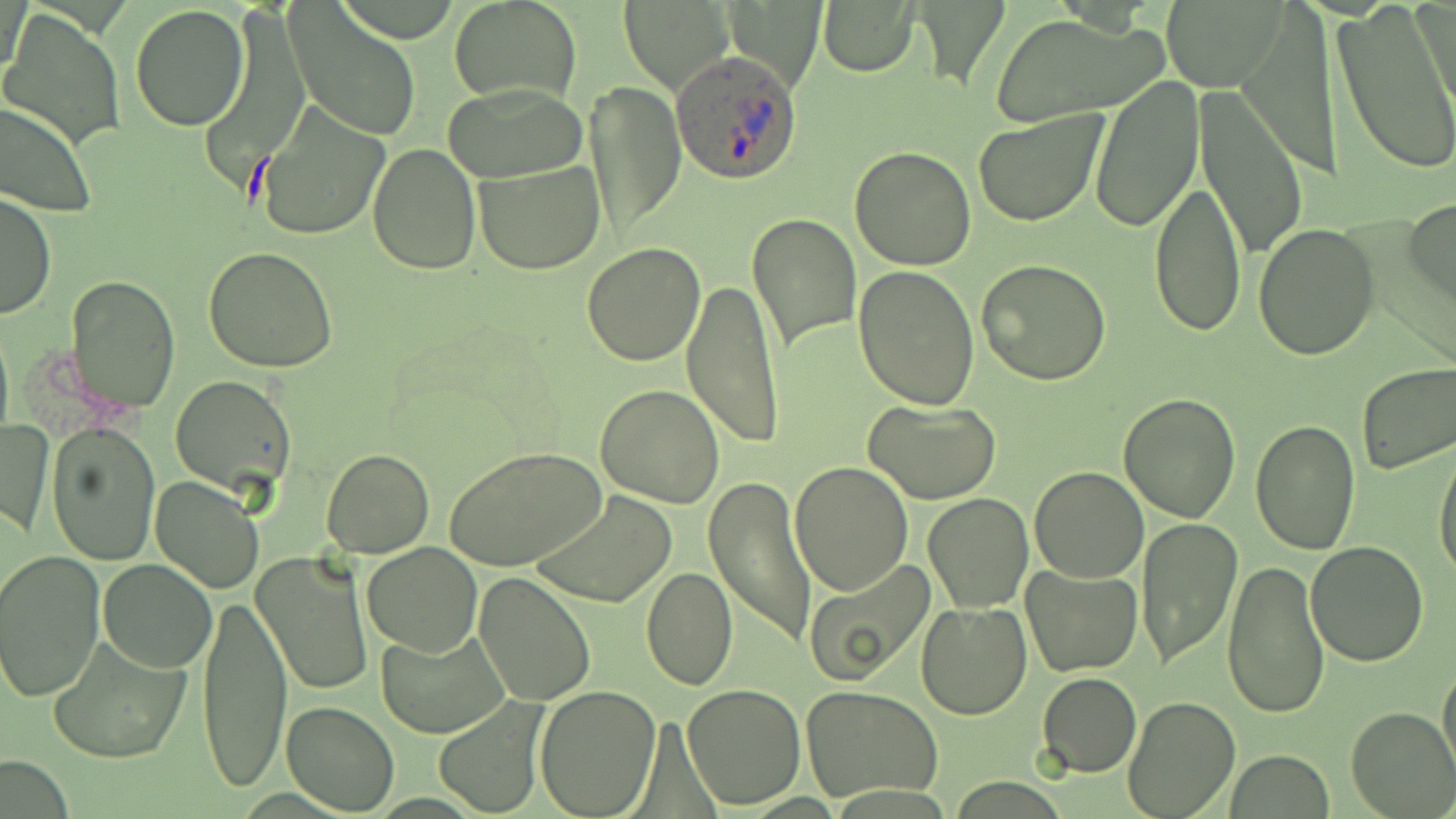
Summary:
  - Coordinate format: approximate bounding boxes as (x1, y1, x2, y2) in pixels
  - Uninfected red blood cell locations: (818, 0, 920, 76), (1414, 0, 1454, 119), (447, 1, 584, 107), (1332, 1, 1456, 178), (618, 2, 735, 96), (1161, 2, 1287, 90), (284, 4, 421, 143), (129, 6, 249, 130), (2, 8, 126, 148), (988, 14, 1166, 125), (1090, 76, 1204, 233), (445, 81, 591, 182), (586, 81, 685, 239), (1194, 85, 1308, 263), (0, 101, 97, 220), (253, 104, 391, 243), (972, 109, 1110, 228), (366, 143, 481, 276), (848, 145, 976, 270), (474, 159, 605, 274), (1148, 177, 1245, 337), (0, 190, 55, 320), (1406, 197, 1456, 309), (747, 211, 861, 355), (1254, 223, 1381, 361), (582, 243, 707, 367), (203, 247, 336, 372), (976, 260, 1111, 386), (854, 263, 980, 410), (64, 274, 180, 414), (683, 279, 786, 447), (1356, 362, 1456, 475), (170, 376, 298, 496), (594, 383, 726, 509), (1118, 391, 1240, 523), (863, 397, 1003, 504), (1, 417, 52, 539), (1249, 420, 1361, 556), (47, 423, 161, 566), (1434, 446, 1456, 582), (446, 447, 606, 574), (321, 449, 434, 557), (789, 460, 912, 595), (1028, 466, 1149, 583), (150, 474, 265, 593), (703, 475, 817, 648), (531, 492, 677, 610), (922, 492, 1034, 612), (1134, 517, 1243, 670), (1305, 540, 1431, 666), (361, 542, 482, 657), (1, 549, 107, 701), (254, 551, 372, 698), (803, 556, 933, 687), (1221, 558, 1330, 720), (98, 559, 216, 672), (1020, 566, 1143, 676), (642, 567, 738, 691), (474, 573, 596, 706), (199, 588, 290, 796), (915, 599, 1033, 720), (379, 624, 510, 738), (49, 636, 193, 766), (1438, 658, 1456, 779), (1037, 671, 1141, 777), (682, 682, 805, 809), (534, 684, 660, 817), (802, 684, 944, 803), (1123, 696, 1241, 819), (433, 699, 549, 817), (281, 701, 400, 815), (1345, 706, 1456, 817), (1227, 750, 1332, 819)
  - Plasmodium ovale-infected red blood cell locations: (670, 53, 803, 182)
  - Slide-level diagnosis: Plasmodium ovale
  - Preparation: thin blood smear
  - Modality: light microscopy
  - Stain: May-Grünwald-Giemsa
  - Field of view: one of a larger specimen
  - Image size: 1456×819 pixels
  - Magnification: 1000x